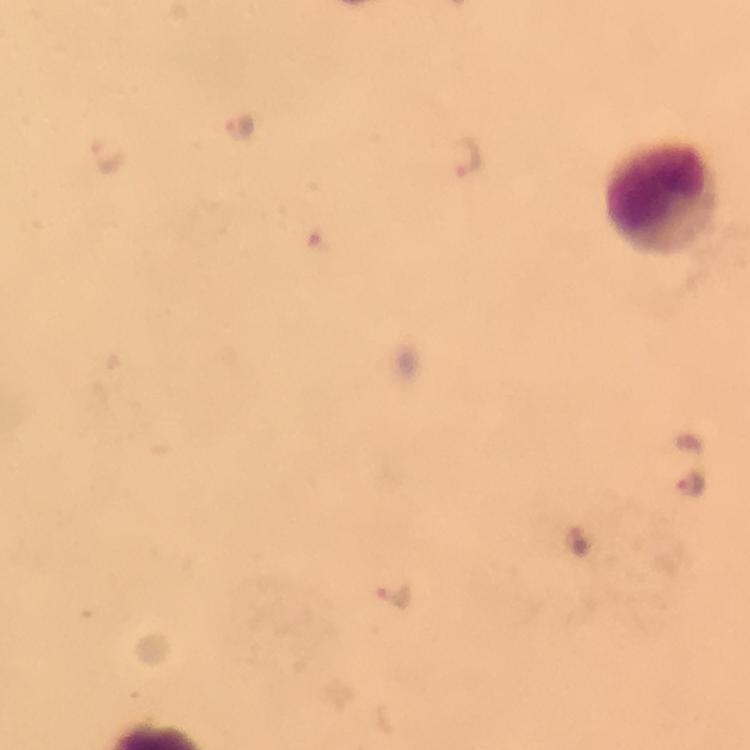
Approximate object centers, in pixels from the top-left corner. Malaria parasite locations: (x=239, y=127), (x=465, y=154), (x=107, y=155), (x=691, y=486), (x=576, y=541), (x=395, y=597). Leukocyte locations: (x=660, y=194). Thick blood smear. A crop from one field of view. Smartphone photograph taken through a microscope. Image is 750×750 pixels. Giemsa-stained preparation. From a diagnostic examination for malaria. Immersion oil was used. At 100x magnification.